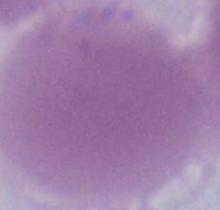

Summary:
  - Magnification: 1000x
  - Identification: erythrocyte
  - Modality: photomicrograph